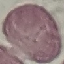

malaria_status: uninfected
stain: Giemsa
capture: smartphone through the microscope eyepiece
image_type: automatically extracted cell patch, resized to 64 × 64 pixels
preparation: thin smear